Classify this cell by malaria status.
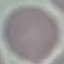
It is uninfected.

Summary:
  - Preparation: thin blood film
  - Stain: Giemsa
  - Capture: smartphone camera at the microscope eyepiece
  - Image type: cell patch, automatically extracted from a larger field of view and resized to 64 × 64 pixels